Classify this cell by malaria status.
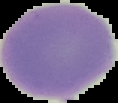
Uninfected.

image size = 118×103 pixels
image type = cell region segmented out of the field of view; surrounding area masked to black
preparation = thin blood smear